State the preparation type.
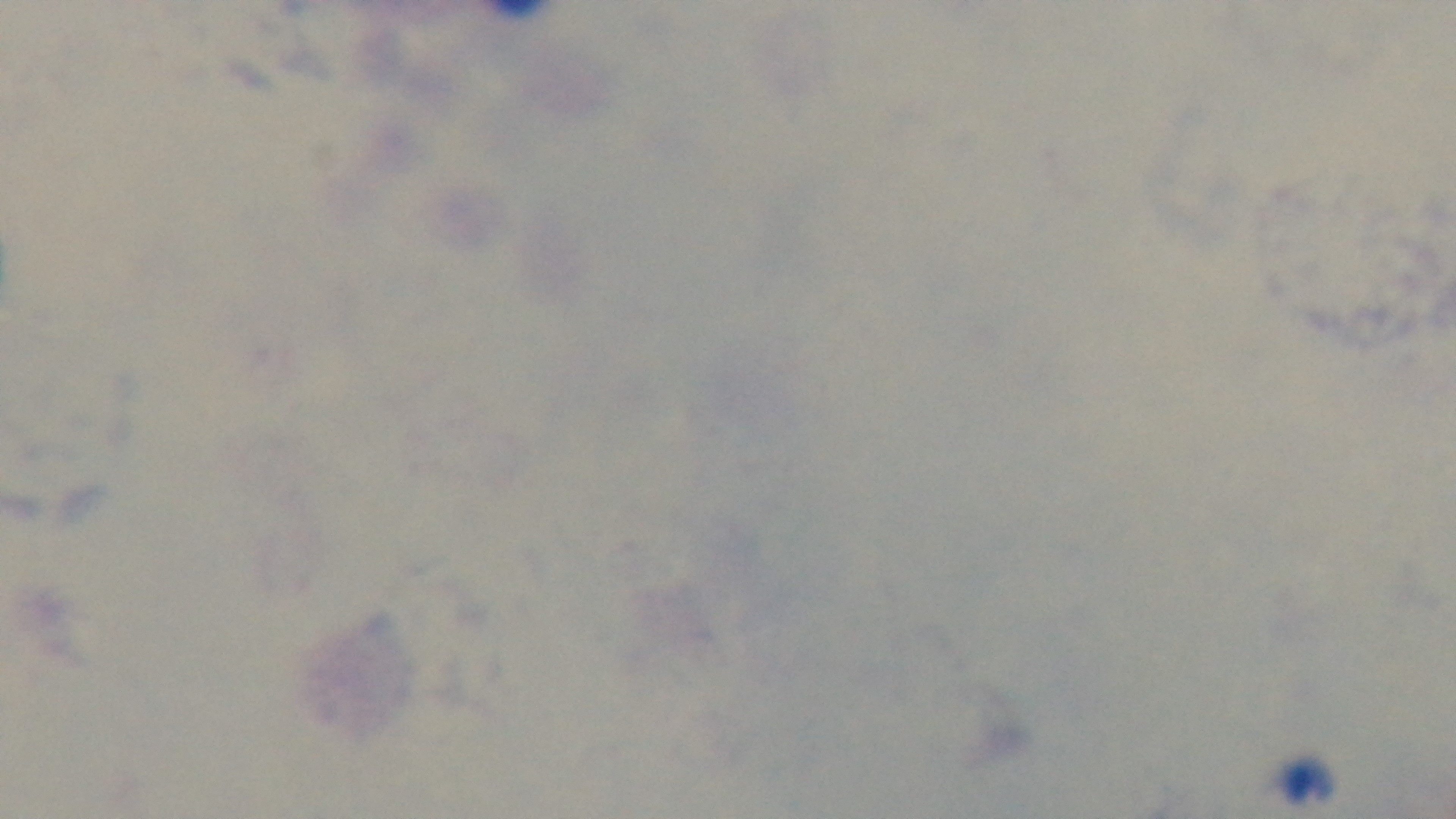

A thick smear.

Summary:
  - Field of view: one from the slide
  - Objective: 100x oil immersion
  - Stain: Giemsa
  - Capture: mounted 4K digital camera
  - Modality: light microscopy
  - Malaria status: uninfected